Locate every P. falciparum parasite and give its life-cycle stage, and locate every leukocyte and any debris.
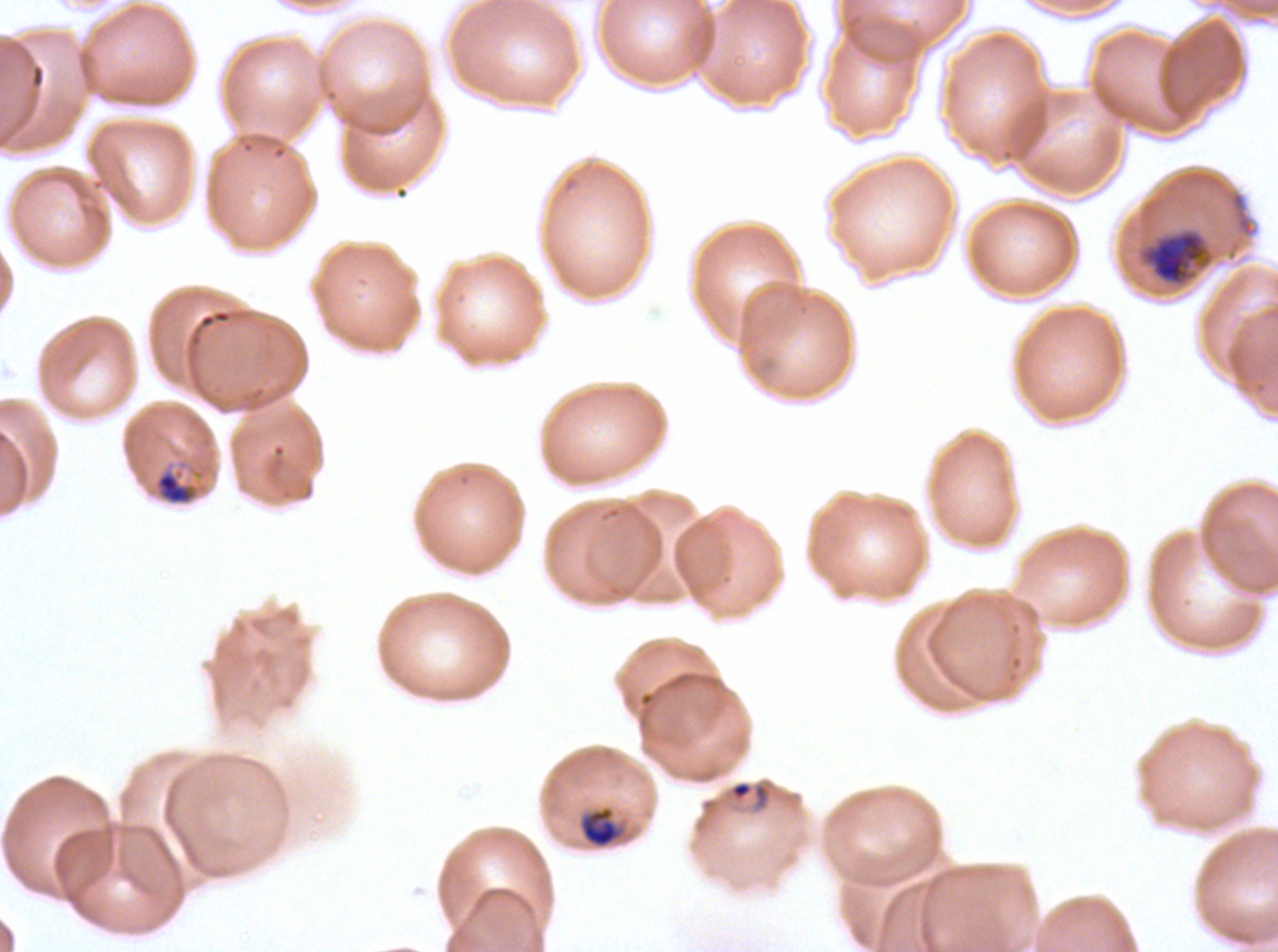

Approximate bounding boxes as (x1, y1, x2, y2) in pixels.
Rings: (728, 780, 771, 810).
Mid trophozoites: (154, 468, 197, 506), (581, 808, 620, 848).
Late trophozoites: (1137, 226, 1215, 287).
No late-ring/early-trophozoite forms, early schizonts, late schizonts, segmenters, gametocytes, leukocytes, or debris observed.

Summary:
  - Preparation: thin blood film
  - Image size: 1278×952 pixels
  - Specimen: P. falciparum from a patient in The Gambia, cultured ex vivo for 24 to 48 hours
  - Field of view: one sub-image of a larger composite
  - Stain: Giemsa
  - Life-cycle stages observed: ring, mid trophozoite, late trophozoite